Assess the morphology of the red blood cells.
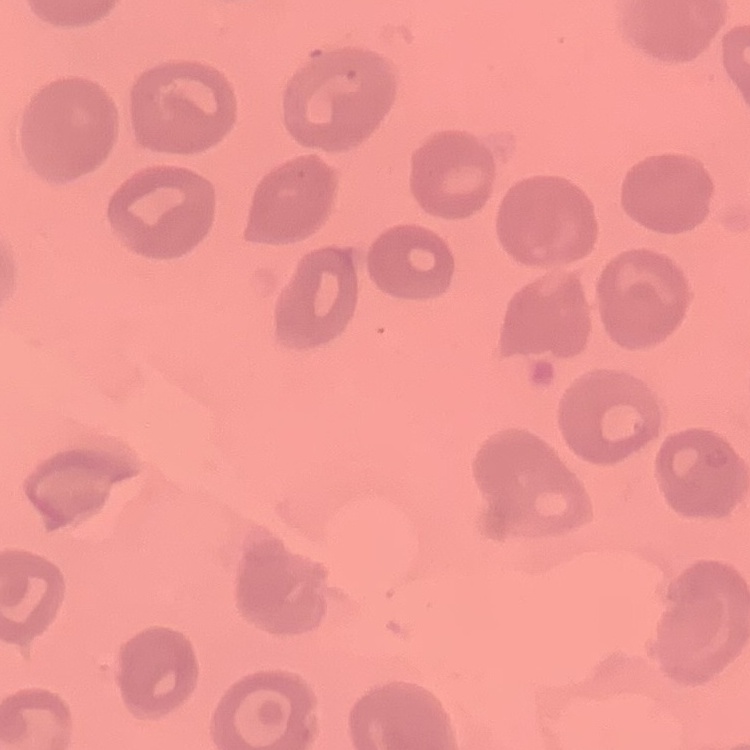

They show no rouleaux formation.

Thin peripheral smear. Stained with either Field's or Giemsa. Square crop of a larger photomicrograph.